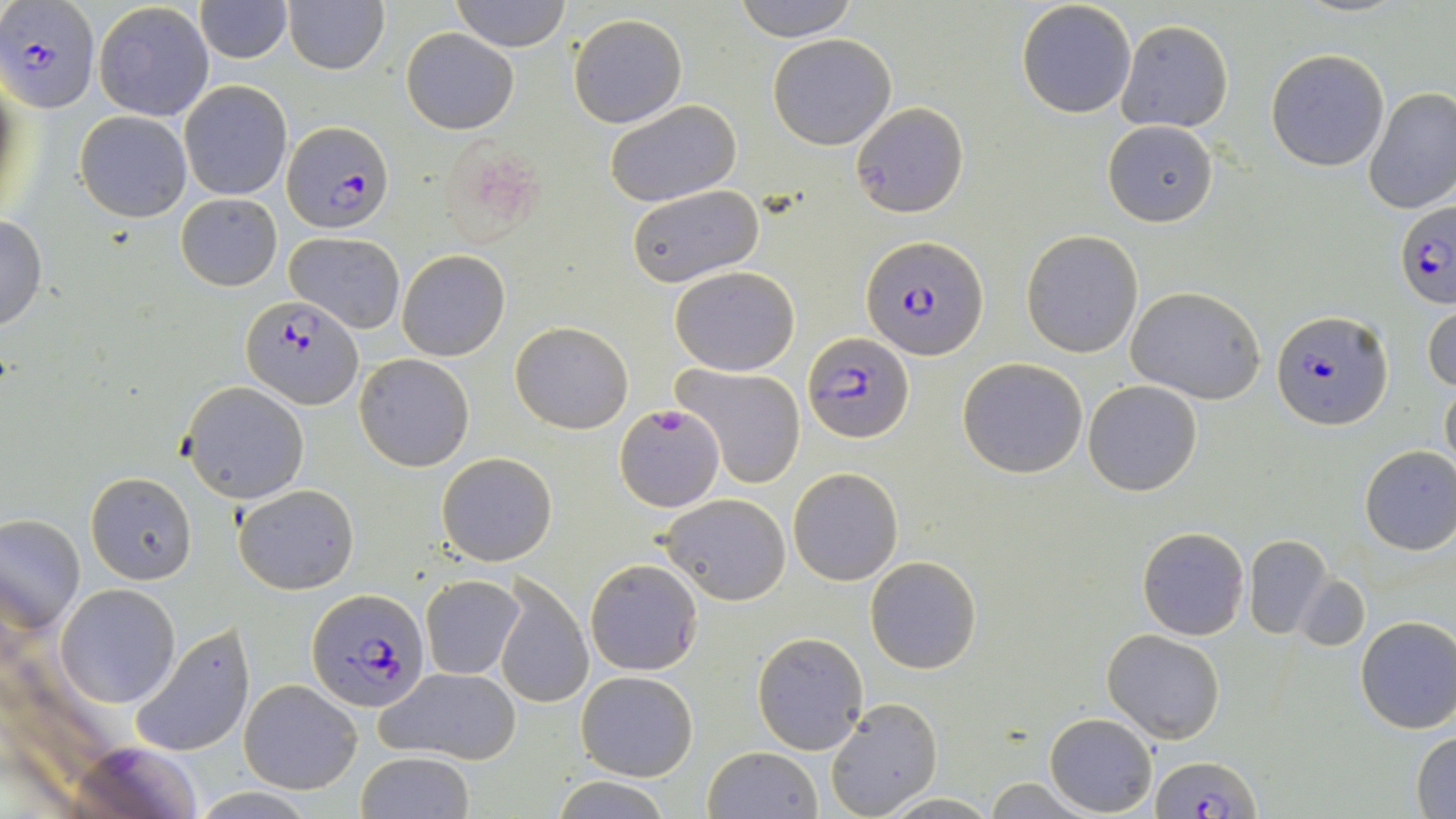

slide-level diagnosis = Plasmodium falciparum
image size = 1456×819 pixels
magnification = 1000x
preparation = thin blood smear
modality = light microscopy
field of view = one of a larger specimen
uninfected red blood cell locations = approximate bounding boxes as (x1, y1, x2, y2) in pixels: (451, 0, 571, 51), (733, 0, 858, 40), (1017, 0, 1138, 119), (285, 1, 388, 75), (93, 2, 215, 122), (193, 2, 292, 62), (567, 13, 688, 128), (1115, 20, 1233, 133), (401, 29, 519, 134), (767, 33, 897, 150), (1265, 49, 1390, 171), (179, 80, 292, 201), (1363, 87, 1456, 214), (604, 101, 742, 207), (850, 101, 968, 219), (75, 111, 192, 221), (1103, 121, 1217, 227), (435, 136, 546, 251), (626, 184, 765, 291), (175, 193, 283, 292), (0, 215, 46, 332), (1020, 229, 1144, 358), (287, 232, 405, 333), (398, 250, 509, 360), (669, 265, 800, 376), (1127, 286, 1266, 403), (1424, 301, 1456, 396), (511, 320, 634, 434), (355, 353, 474, 471), (957, 357, 1089, 478), (672, 362, 806, 489), (1084, 380, 1202, 496), (1439, 380, 1455, 475), (178, 381, 310, 502), (1358, 445, 1456, 556), (435, 452, 557, 567), (788, 466, 903, 586), (85, 472, 197, 585), (234, 483, 359, 594), (657, 493, 791, 605), (0, 513, 85, 636), (1137, 526, 1248, 640), (1245, 534, 1332, 639), (865, 556, 982, 674), (585, 558, 704, 676), (493, 574, 593, 710), (419, 575, 525, 680), (1294, 575, 1369, 651), (56, 584, 180, 706), (1356, 616, 1456, 733), (131, 624, 257, 757), (1102, 629, 1226, 744), (753, 632, 868, 754), (375, 666, 522, 765), (575, 670, 698, 781), (238, 679, 363, 792), (826, 696, 942, 818), (1045, 713, 1157, 815), (1412, 730, 1456, 817), (701, 747, 822, 819), (355, 752, 474, 819), (984, 776, 1093, 817), (552, 777, 672, 817), (882, 793, 1001, 818)
Plasmodium falciparum-infected red blood cell locations = approximate bounding boxes as (x1, y1, x2, y2) in pixels: (0, 3, 100, 112), (281, 121, 394, 233), (1395, 201, 1456, 309), (863, 236, 989, 359), (239, 293, 362, 411), (1271, 308, 1391, 430), (803, 333, 913, 443), (614, 406, 722, 511), (306, 589, 429, 714), (1153, 753, 1260, 818)
stain = May-Grünwald-Giemsa